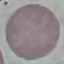
Summary:
  - Malaria status: uninfected
  - Stain: Giemsa
  - Preparation: thin blood smear
  - Image type: cell patch, automatically extracted from a larger field of view and resized to 64 × 64 pixels
  - Capture: smartphone through the microscope eyepiece